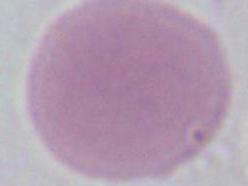

Micrograph. An erythrocyte is seen. Captured at 1000x magnification.